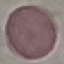

result = negative for malaria parasites
capture = smartphone through the microscope eyepiece
preparation = thin blood film
stain = Giemsa
image type = cell patch, automatically extracted from a larger field of view and resized to 64 × 64 pixels